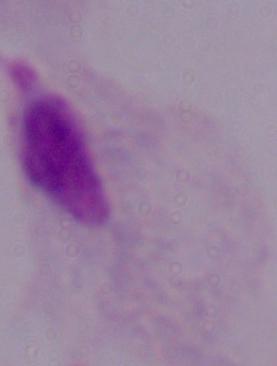

identification = trichomonad
magnification = 1000x
modality = photomicrograph